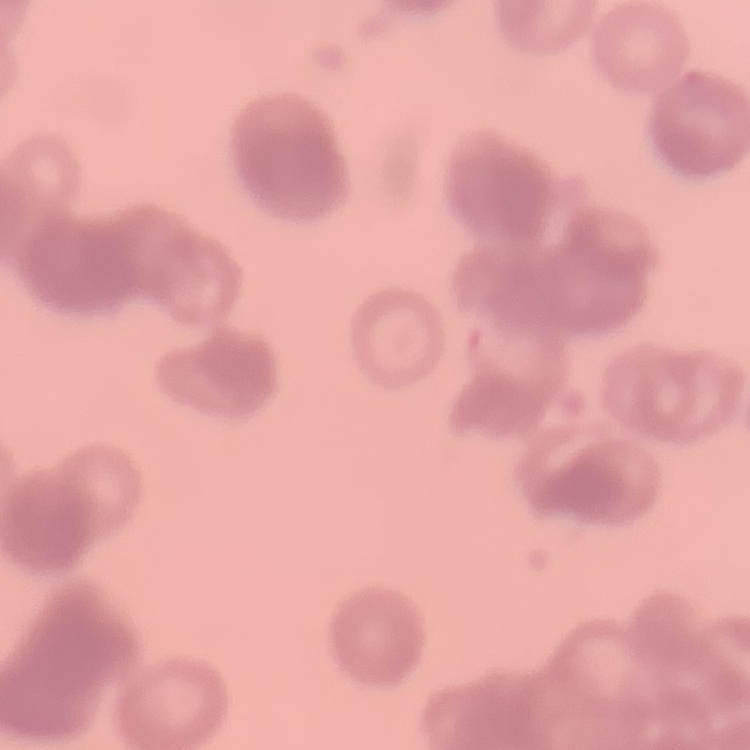

red blood cell morphology = rouleaux formation
preparation = thin blood film
image type = one tile cut from a larger photomicrograph
stain = Field's or Giemsa